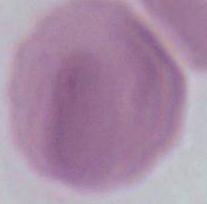
magnification = 1000x
modality = photomicrograph
identification = red blood cell